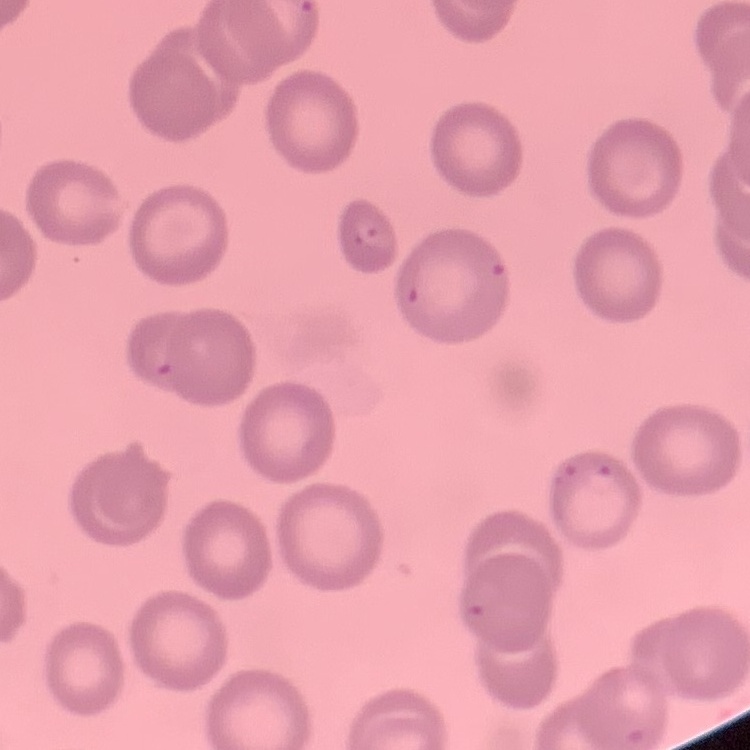

The red blood cells show no rouleaux formation. Square crop of a larger photomicrograph. Thin peripheral smear. Stained with either Field's or Giemsa.